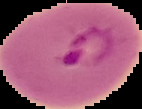
{
  "image_size": "142×109 pixels",
  "malaria_status": "parasitized",
  "preparation": "thin blood film",
  "image_type": "cell region segmented out of the field of view; surrounding area masked to black"
}